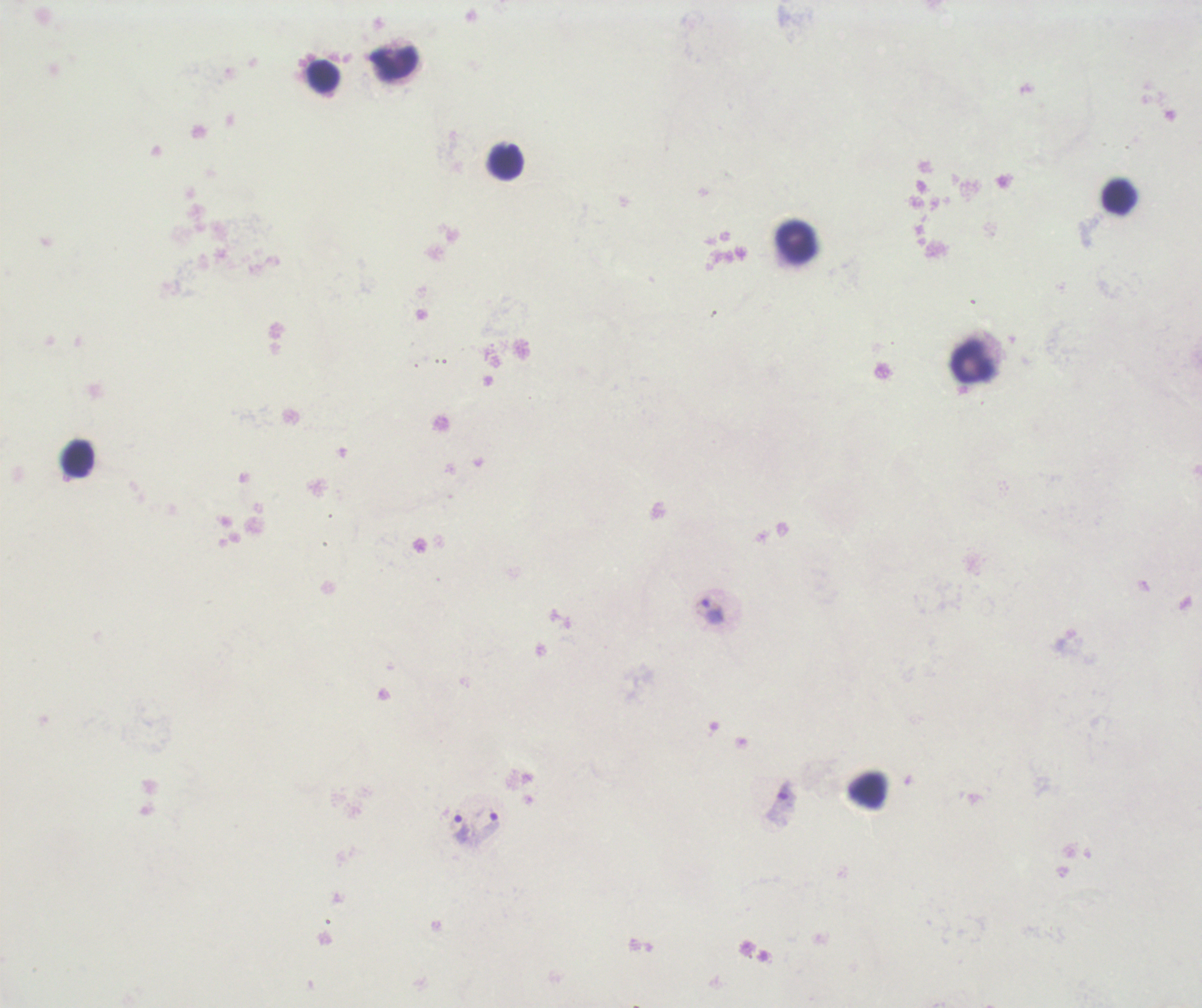
coordinate format = approximate centers as {x, y} in pixels
leukocyte locations = {394, 64}, {322, 76}, {507, 161}, {1119, 196}, {798, 243}, {973, 361}, {76, 457}, {867, 790}
trophozoite locations = {709, 611}, {780, 806}, {487, 827}, {461, 828}
preparation = thick blood smear
stain = Romanowsky
magnification = 100x
result = malaria parasites detected
context = previously used in an actual diagnosis
background quality = unsatisfactory
coloration quality = bad
field of view = one from this slide
image size = 1202×1008 pixels